Name the cell type shown.
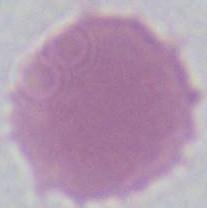

An erythrocyte.

Summary:
  - Modality: photomicrograph
  - Magnification: 1000x